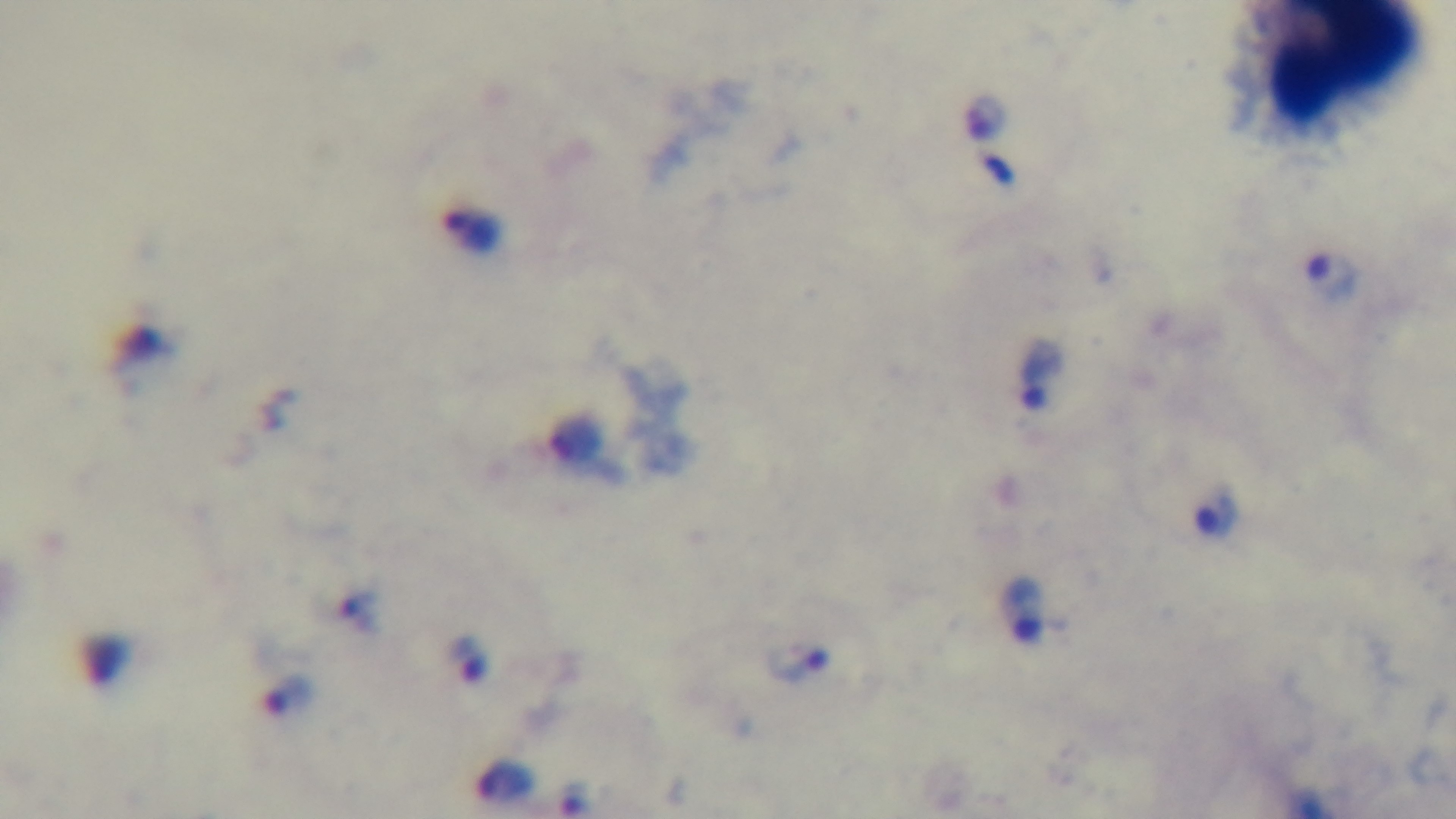

Summary:
  - Field of view: one from the slide
  - Capture: mounted 4K digital camera
  - Stain: Giemsa
  - Objective: 100x oil immersion
  - Malaria status: positive
  - Preparation: thick blood film
  - Modality: light microscopy